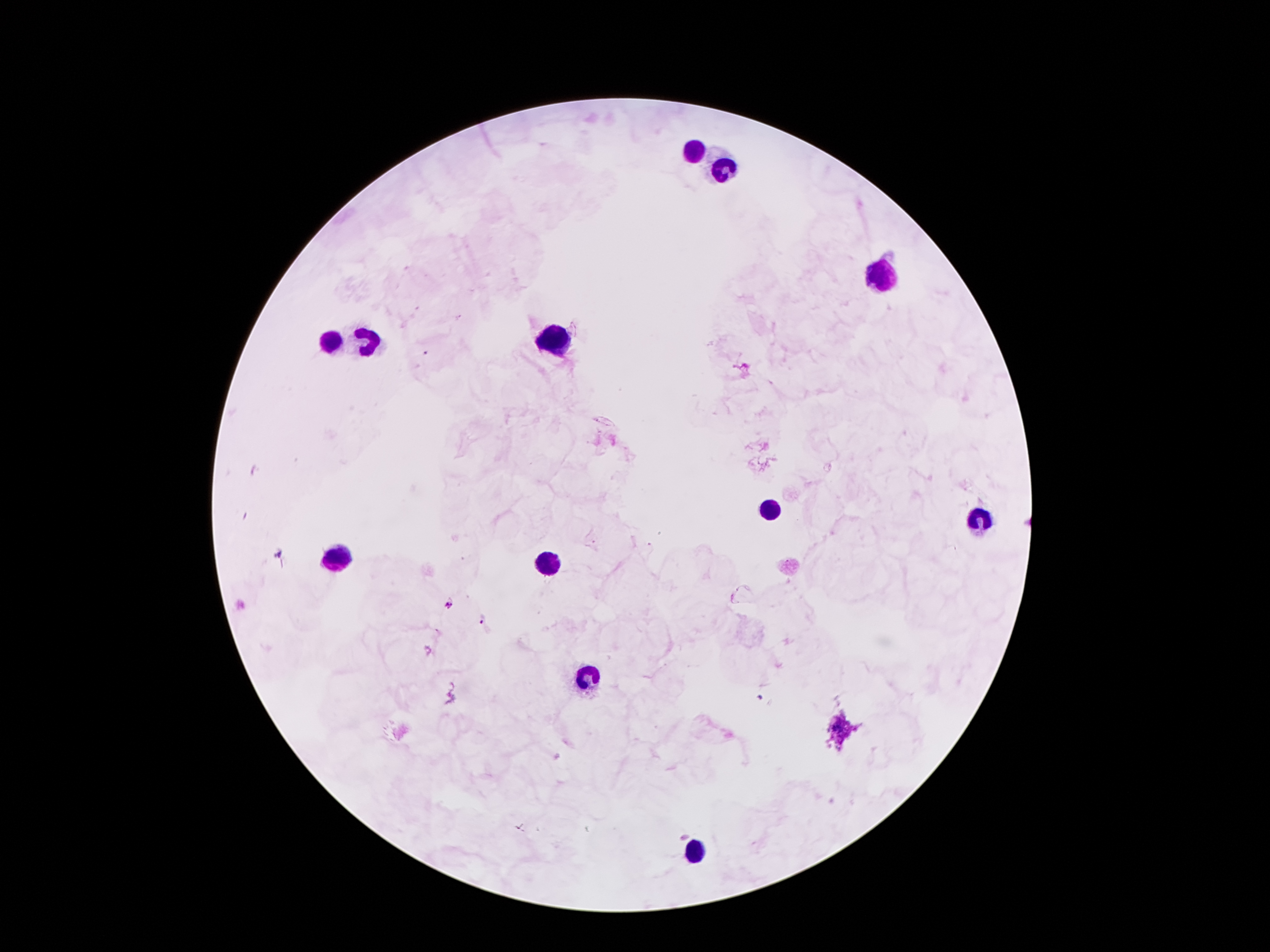
Approximate centers as (x, y) in pixels. Malaria parasite locations: (448, 603), (484, 618), (759, 697). Leukocyte locations: (694, 148), (723, 167), (879, 273), (327, 340), (366, 340), (553, 340), (769, 510), (978, 517), (337, 556), (548, 563), (586, 676), (699, 851). 100x magnification. Thick blood film. Patient malaria status: positive for Plasmodium falciparum. Giemsa stain. Photographed through the microscope eyepiece with a smartphone camera. Image is 1270×952 pixels. Single field of view.